State the blood parasite species.
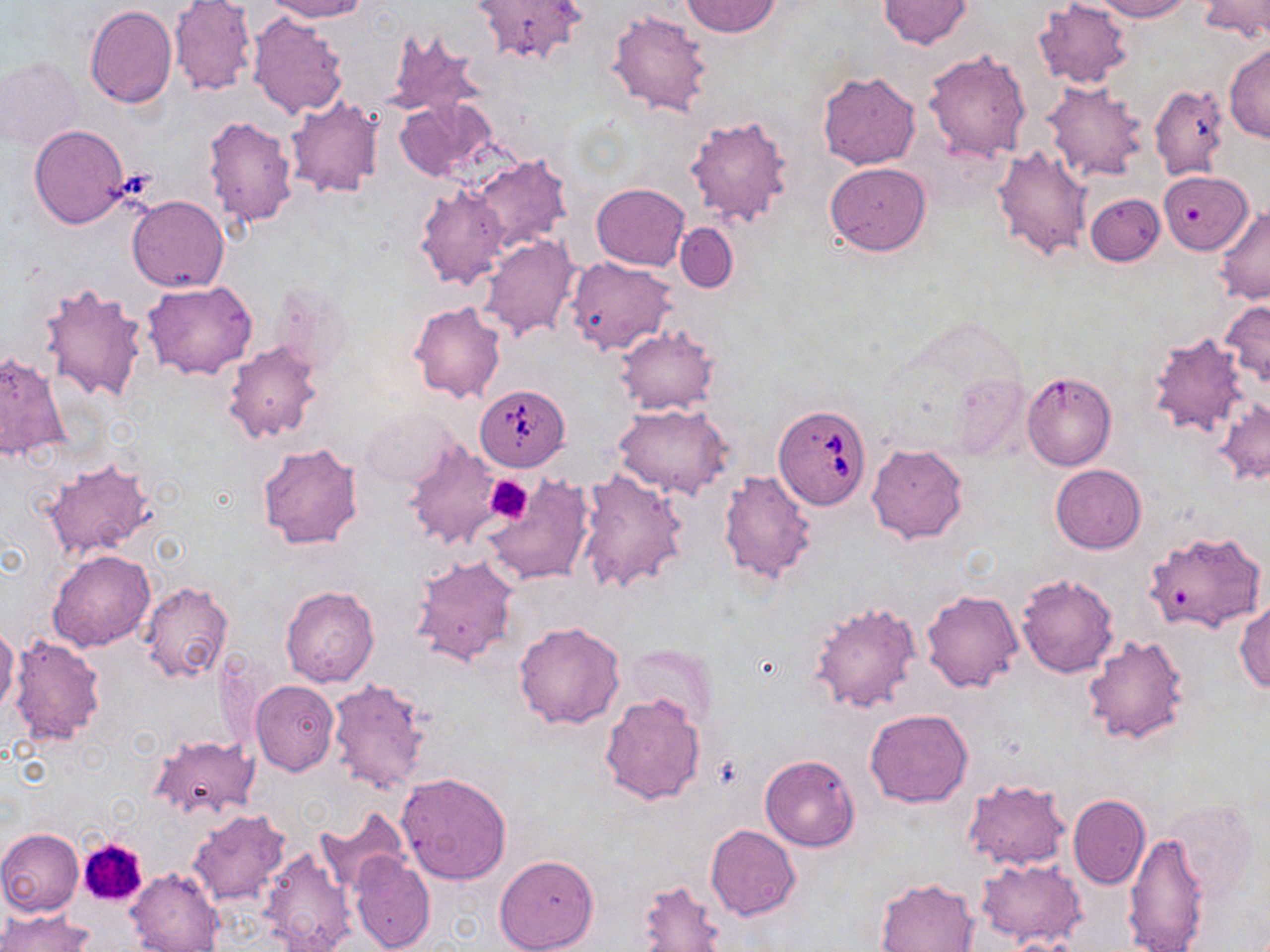

Babesia divergens.

Summary:
  - Coordinate format: approximate bounding boxes as named x1/y1/x2/y2 corners in pixels
  - Babesia divergens-infected red blood cell locations: (x1=475, y1=385, x2=570, y2=470), (x1=773, y1=403, x2=872, y2=512)
  - Uninfected red blood cell locations: (x1=261, y1=0, x2=367, y2=22), (x1=472, y1=0, x2=587, y2=65), (x1=878, y1=0, x2=974, y2=49), (x1=1032, y1=0, x2=1135, y2=89), (x1=1086, y1=0, x2=1193, y2=21), (x1=1199, y1=0, x2=1270, y2=44), (x1=680, y1=1, x2=781, y2=37), (x1=170, y1=2, x2=257, y2=98), (x1=84, y1=5, x2=177, y2=108), (x1=606, y1=9, x2=713, y2=117), (x1=248, y1=14, x2=348, y2=119), (x1=383, y1=26, x2=488, y2=122), (x1=1224, y1=43, x2=1270, y2=143), (x1=923, y1=49, x2=1033, y2=162), (x1=1, y1=57, x2=84, y2=151), (x1=818, y1=72, x2=919, y2=170), (x1=1043, y1=82, x2=1149, y2=183), (x1=1150, y1=83, x2=1230, y2=180), (x1=394, y1=96, x2=499, y2=184), (x1=285, y1=98, x2=384, y2=199), (x1=684, y1=113, x2=794, y2=229), (x1=203, y1=115, x2=298, y2=227), (x1=29, y1=124, x2=130, y2=228), (x1=992, y1=144, x2=1094, y2=261), (x1=469, y1=153, x2=571, y2=252), (x1=825, y1=162, x2=931, y2=257), (x1=1162, y1=177, x2=1258, y2=258), (x1=592, y1=183, x2=689, y2=271), (x1=415, y1=184, x2=510, y2=290), (x1=1085, y1=193, x2=1164, y2=266), (x1=127, y1=195, x2=229, y2=292), (x1=1214, y1=205, x2=1270, y2=302), (x1=676, y1=222, x2=737, y2=292), (x1=478, y1=234, x2=581, y2=342), (x1=566, y1=257, x2=676, y2=356), (x1=143, y1=280, x2=258, y2=378), (x1=38, y1=281, x2=149, y2=403), (x1=271, y1=281, x2=355, y2=378), (x1=1220, y1=299, x2=1270, y2=388), (x1=408, y1=301, x2=506, y2=404), (x1=614, y1=325, x2=718, y2=414), (x1=1148, y1=332, x2=1252, y2=440), (x1=222, y1=340, x2=324, y2=444), (x1=0, y1=351, x2=69, y2=462), (x1=1027, y1=370, x2=1115, y2=473), (x1=949, y1=373, x2=1032, y2=461), (x1=1215, y1=398, x2=1270, y2=484), (x1=613, y1=403, x2=734, y2=500), (x1=360, y1=407, x2=458, y2=491), (x1=405, y1=441, x2=505, y2=551), (x1=257, y1=443, x2=364, y2=550), (x1=867, y1=444, x2=968, y2=543), (x1=41, y1=457, x2=157, y2=560), (x1=1050, y1=464, x2=1147, y2=553), (x1=576, y1=470, x2=687, y2=594), (x1=718, y1=470, x2=818, y2=585), (x1=485, y1=480, x2=594, y2=589), (x1=1144, y1=529, x2=1266, y2=634), (x1=48, y1=549, x2=156, y2=650), (x1=409, y1=554, x2=520, y2=668), (x1=1015, y1=572, x2=1120, y2=679), (x1=139, y1=580, x2=232, y2=683), (x1=279, y1=585, x2=379, y2=688), (x1=921, y1=587, x2=1024, y2=693), (x1=814, y1=593, x2=1024, y2=701), (x1=809, y1=598, x2=922, y2=716), (x1=1234, y1=600, x2=1270, y2=693), (x1=513, y1=622, x2=625, y2=729), (x1=0, y1=627, x2=20, y2=716), (x1=9, y1=635, x2=106, y2=747), (x1=1082, y1=635, x2=1191, y2=745), (x1=627, y1=644, x2=719, y2=726), (x1=326, y1=678, x2=429, y2=796), (x1=252, y1=680, x2=339, y2=776), (x1=600, y1=694, x2=706, y2=805), (x1=864, y1=709, x2=972, y2=808), (x1=147, y1=734, x2=258, y2=821), (x1=760, y1=754, x2=861, y2=852), (x1=396, y1=772, x2=512, y2=886), (x1=962, y1=777, x2=1072, y2=871), (x1=1068, y1=793, x2=1149, y2=891), (x1=1165, y1=798, x2=1260, y2=903), (x1=316, y1=806, x2=411, y2=896), (x1=188, y1=809, x2=291, y2=906), (x1=705, y1=824, x2=801, y2=921), (x1=0, y1=828, x2=85, y2=916), (x1=1122, y1=831, x2=1211, y2=952), (x1=259, y1=843, x2=358, y2=952), (x1=351, y1=852, x2=435, y2=951), (x1=493, y1=854, x2=599, y2=952), (x1=977, y1=859, x2=1087, y2=948), (x1=126, y1=869, x2=224, y2=951), (x1=875, y1=876, x2=980, y2=951), (x1=634, y1=879, x2=727, y2=950), (x1=0, y1=907, x2=93, y2=952)
  - Platelet locations: (x1=485, y1=475, x2=532, y2=524), (x1=76, y1=837, x2=149, y2=909)
  - Magnification: 1000x
  - Field of view: one of a larger specimen
  - Preparation: thin blood smear
  - Image size: 1270×952 pixels
  - Stain: May-Grünwald-Giemsa
  - Modality: light microscopy